Comment on the morphology of the red blood cells.
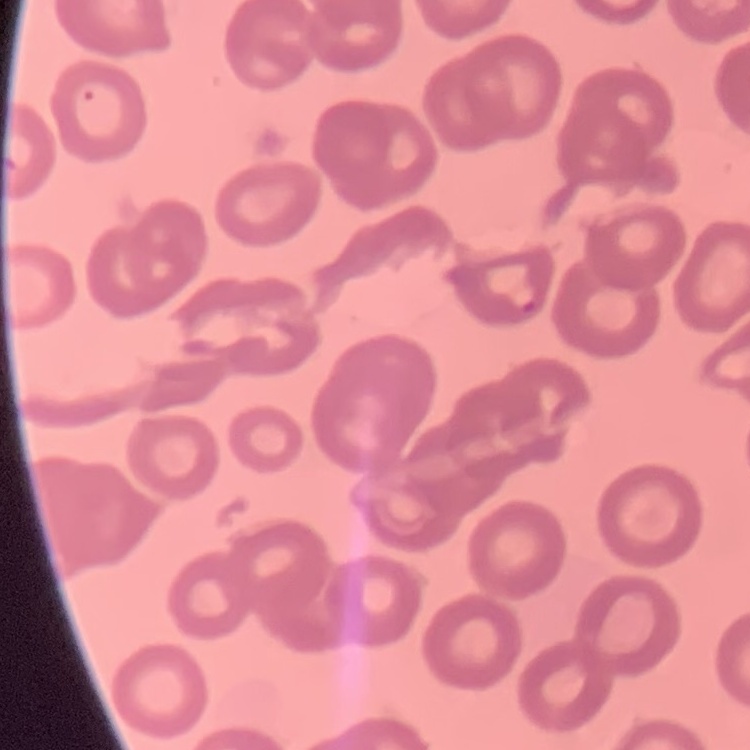
They show no rouleaux formation.

Summary:
  - Preparation: thin blood smear
  - Image type: square crop of a larger photomicrograph
  - Stain: Field's or Giemsa